Assess this cell for malaria.
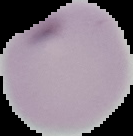
It is uninfected.

Summary:
  - Image type: cell region segmented out of the field of view; surrounding area masked to black
  - Image size: 133×136 pixels
  - Preparation: thin blood smear